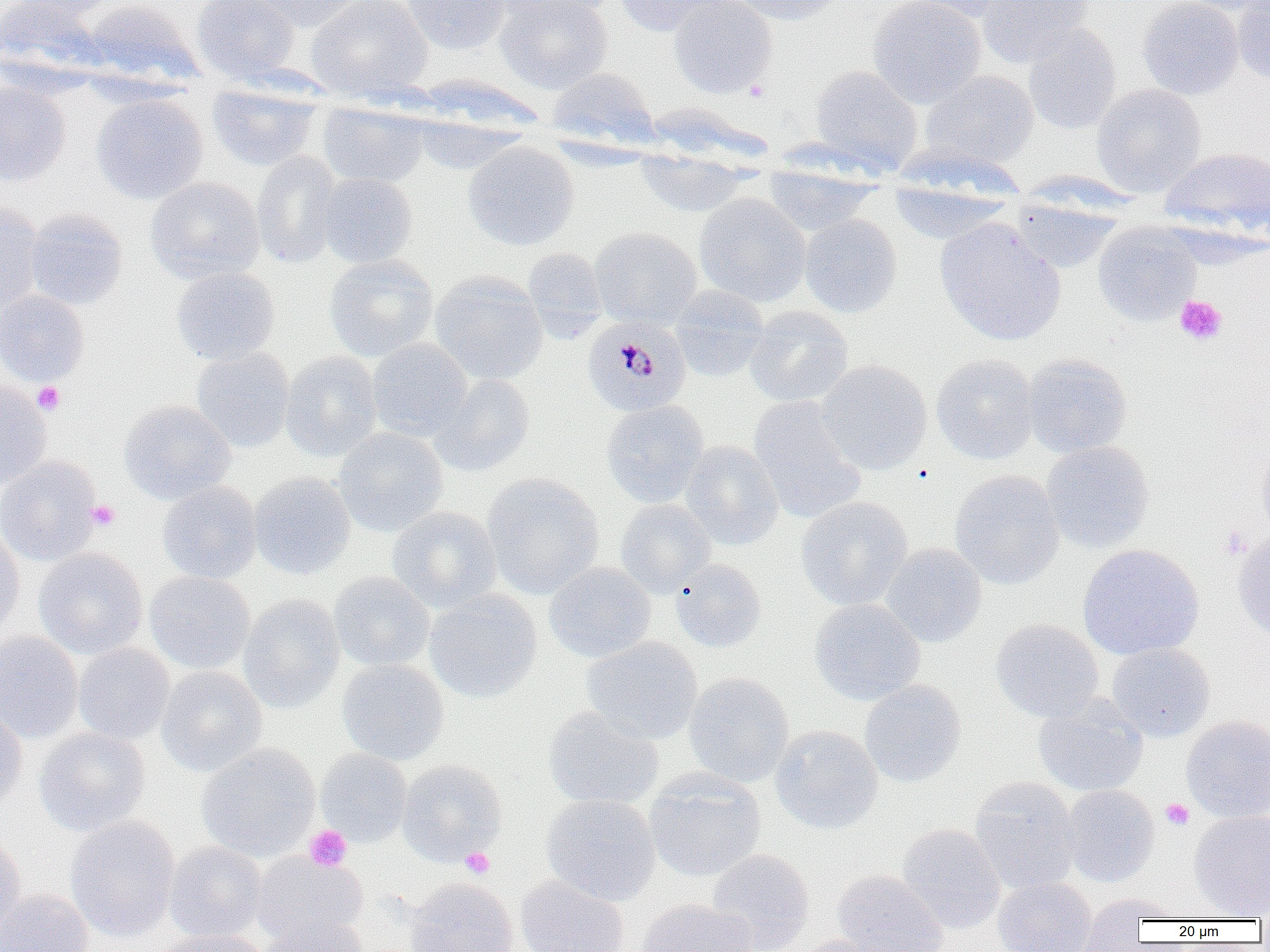

Approximate bounding boxes as [x1, y1, x2, y2] in pixels. Uninfected red blood cell locations: [0, 0, 104, 83], [10, 0, 120, 18], [191, 0, 300, 82], [241, 0, 371, 32], [306, 0, 433, 100], [401, 0, 511, 54], [494, 0, 617, 24], [495, 0, 613, 93], [611, 0, 731, 36], [669, 0, 778, 98], [730, 0, 844, 26], [867, 0, 986, 108], [903, 0, 1009, 23], [977, 0, 1095, 68], [1137, 0, 1244, 100], [1164, 0, 1270, 13], [80, 1, 202, 88], [1233, 1, 1270, 88], [1022, 23, 1121, 135], [810, 64, 924, 176], [545, 67, 659, 151], [921, 70, 1039, 167], [0, 81, 70, 186], [1091, 83, 1207, 197], [207, 85, 321, 171], [90, 93, 209, 204], [318, 102, 429, 189], [409, 108, 529, 175], [462, 141, 579, 250], [1160, 147, 1269, 238], [635, 148, 752, 218], [250, 150, 342, 270], [763, 161, 877, 236], [318, 172, 417, 268], [145, 176, 265, 285], [888, 178, 1012, 245], [693, 193, 812, 307], [1009, 195, 1122, 273], [0, 202, 45, 314], [25, 208, 128, 310], [799, 214, 902, 318], [935, 217, 1066, 346], [1092, 222, 1202, 325], [590, 228, 703, 329], [522, 248, 608, 342], [324, 254, 438, 362], [171, 267, 280, 365], [429, 270, 548, 384], [670, 285, 770, 383], [0, 290, 89, 386], [744, 305, 853, 407], [367, 338, 473, 442], [192, 347, 294, 454], [280, 351, 382, 462], [1022, 353, 1133, 458], [931, 354, 1039, 464], [817, 360, 932, 474], [430, 373, 536, 476], [0, 379, 51, 489], [747, 395, 868, 524], [118, 400, 236, 504], [601, 400, 709, 507], [333, 427, 448, 536], [1257, 439, 1270, 540], [680, 441, 784, 550], [1041, 441, 1155, 554], [0, 456, 102, 566], [949, 470, 1064, 589], [249, 472, 355, 580], [482, 473, 604, 598], [158, 480, 262, 583], [796, 497, 912, 611], [615, 499, 715, 598], [386, 506, 502, 612], [0, 526, 25, 642], [1232, 529, 1270, 639], [882, 543, 987, 647], [1077, 544, 1205, 659], [33, 547, 148, 660], [670, 558, 767, 653], [544, 562, 656, 662], [145, 571, 255, 673], [329, 571, 434, 672], [425, 589, 542, 703], [238, 594, 345, 713], [809, 598, 925, 706], [990, 619, 1104, 722], [0, 631, 83, 742], [581, 637, 702, 744], [1106, 642, 1215, 742], [73, 643, 175, 744], [336, 659, 449, 765], [156, 666, 267, 776], [684, 672, 794, 787], [860, 680, 966, 788], [1033, 695, 1149, 797], [543, 706, 664, 810], [0, 707, 27, 811], [1181, 715, 1270, 822], [770, 724, 883, 834], [34, 727, 150, 836], [197, 744, 320, 862], [315, 749, 412, 847], [397, 759, 507, 865], [645, 769, 766, 882], [969, 777, 1081, 895], [1061, 785, 1158, 887], [541, 793, 660, 905], [1189, 811, 1270, 917], [65, 815, 180, 942], [897, 823, 1005, 934], [0, 828, 26, 935], [164, 841, 267, 943], [707, 849, 813, 952], [251, 851, 368, 947], [833, 869, 949, 952], [515, 874, 630, 952], [404, 877, 519, 952], [994, 877, 1096, 952], [0, 888, 95, 952], [1077, 893, 1167, 951], [1085, 893, 1183, 923], [637, 899, 757, 952], [258, 914, 370, 952], [152, 928, 274, 952], [790, 935, 901, 952]. Platelet locations: [744, 79, 769, 101], [1174, 295, 1227, 345], [32, 381, 65, 415], [86, 500, 120, 531], [1220, 526, 1249, 559], [1160, 798, 1195, 830], [304, 825, 352, 872], [460, 847, 494, 878]. Plasmodium malariae-infected red blood cell locations: [583, 316, 690, 417]. Slide-level diagnosis: Plasmodium malariae. Thin blood film. Image is 1270×952 pixels. One field of a larger specimen. Optical microscopy. Captured at 1000x magnification.